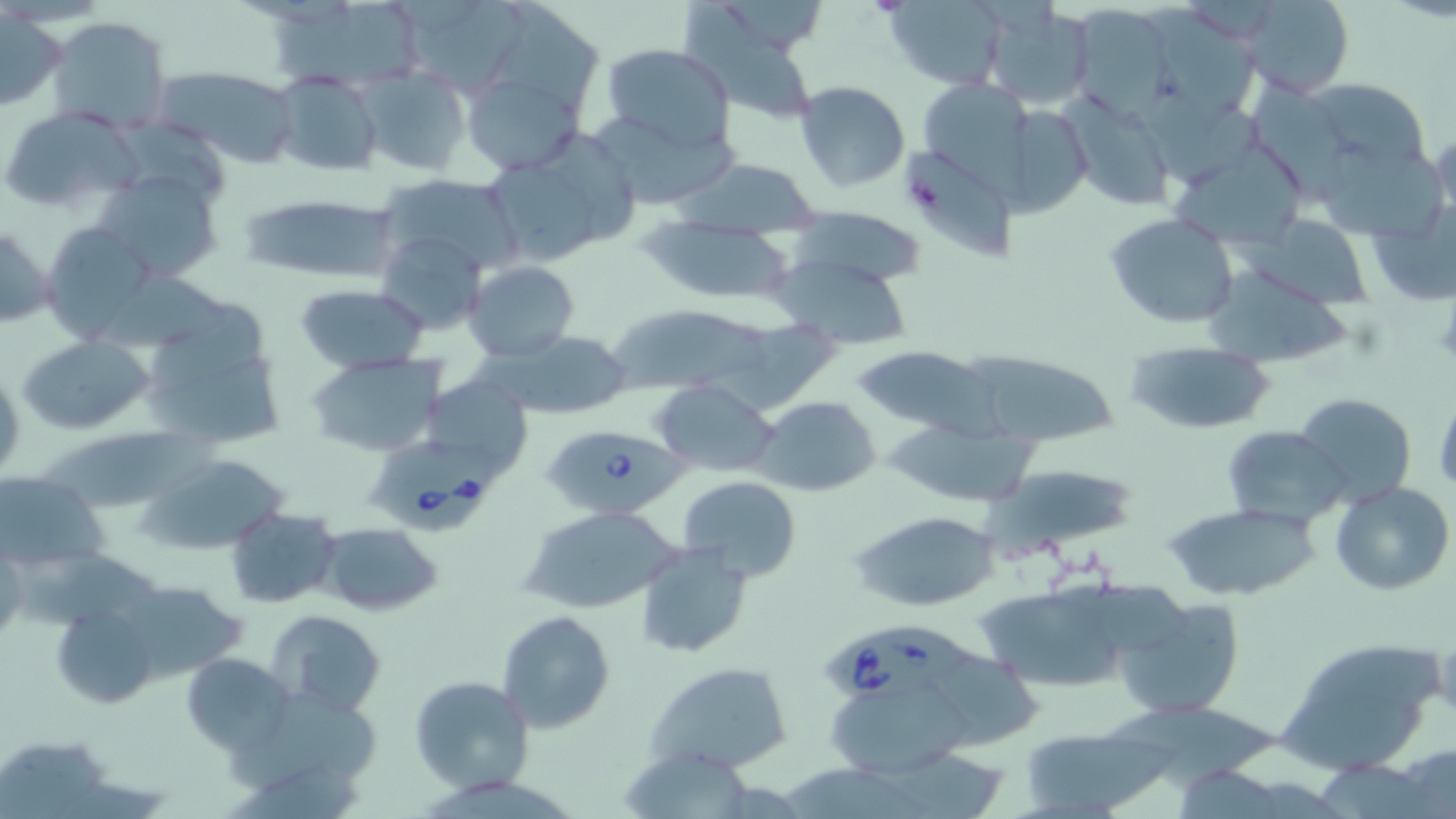
slide_level_diagnosis: Babesia divergens
image_size: 1456×819 pixels
field_of_view: one of a larger specimen
modality: optical microscopy
platelet_locations: 'approximate bounding boxes as (x1, y1, x2, y2) in pixels: (907, 174, 947, 216)'
babesia_divergens_infected_red_blood_cell_locations: 'approximate bounding boxes as (x1, y1, x2, y2) in pixels: (540, 421, 685, 518), (368, 438, 504, 539), (820, 619, 980, 695)'
uninfected_red_blood_cell_locations: 'approximate bounding boxes as (x1, y1, x2, y2) in pixels: (397, 0, 531, 95), (498, 0, 605, 111), (679, 0, 815, 128), (880, 0, 1011, 88), (1238, 0, 1354, 97), (267, 4, 433, 94), (980, 4, 1095, 110), (1075, 6, 1175, 122), (1149, 11, 1259, 119), (1, 12, 67, 111), (46, 16, 174, 134), (600, 43, 737, 154), (358, 66, 471, 176), (154, 67, 301, 166), (461, 68, 586, 176), (270, 72, 383, 177), (924, 75, 1042, 207), (1305, 77, 1429, 172), (795, 81, 910, 194), (1256, 82, 1357, 207), (1135, 89, 1267, 189), (1062, 97, 1178, 210), (1011, 104, 1087, 219), (1, 106, 138, 210), (595, 115, 748, 207), (116, 120, 227, 208), (1429, 126, 1456, 227), (548, 133, 640, 242), (1171, 139, 1310, 250), (1320, 146, 1448, 242), (905, 152, 1018, 262), (683, 157, 823, 235), (493, 164, 599, 265), (96, 168, 225, 282), (375, 175, 524, 274), (240, 191, 397, 283), (1363, 196, 1455, 309), (787, 207, 928, 288), (1104, 212, 1239, 330), (1245, 213, 1376, 310), (643, 220, 800, 305), (0, 221, 53, 331), (42, 222, 158, 344), (374, 230, 488, 335), (774, 254, 912, 349), (463, 259, 580, 361), (87, 263, 230, 349), (1206, 265, 1351, 369), (295, 284, 431, 374), (603, 308, 774, 384), (137, 313, 288, 451), (730, 316, 842, 415), (488, 329, 634, 419), (17, 332, 156, 437), (1123, 337, 1277, 436), (850, 345, 997, 436), (968, 353, 1120, 446), (306, 354, 445, 457), (425, 374, 535, 486), (650, 380, 780, 480), (1295, 392, 1416, 506), (1434, 393, 1456, 496), (752, 395, 881, 495), (42, 422, 223, 511), (883, 422, 1038, 509), (1220, 425, 1350, 528), (139, 454, 287, 554), (991, 460, 1143, 550), (1, 472, 106, 570), (678, 475, 802, 583), (1330, 482, 1455, 596), (1163, 502, 1319, 602), (521, 506, 681, 614), (224, 508, 342, 608), (853, 509, 1001, 613), (317, 522, 444, 617), (634, 542, 753, 658), (1, 544, 26, 644), (27, 552, 167, 627), (116, 580, 246, 682), (976, 581, 1146, 694), (1115, 595, 1247, 719), (50, 603, 160, 709), (267, 609, 388, 717), (497, 609, 615, 734), (1281, 639, 1443, 774), (181, 653, 296, 757), (644, 661, 793, 774), (409, 674, 534, 795), (826, 674, 974, 779), (228, 691, 376, 790), (1106, 695, 1277, 789), (1020, 725, 1165, 818), (5, 734, 112, 814), (1393, 742, 1456, 819), (619, 747, 761, 819), (880, 748, 1011, 817), (224, 762, 369, 819), (1178, 762, 1287, 819), (779, 766, 928, 819)'
stain: May-Grünwald-Giemsa
magnification: 1000x
preparation: thin blood film